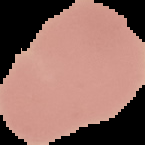
Image is 145×145 pixels. From a thin blood smear. The area outside the segmented cell region is set to black. Result: negative for Plasmodium parasites.